Classify this cell by malaria status.
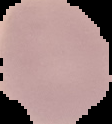
Uninfected.

{
  "preparation": "thin blood smear",
  "image_type": "segmented cell region on a black background",
  "image_size": "112×124 pixels"
}